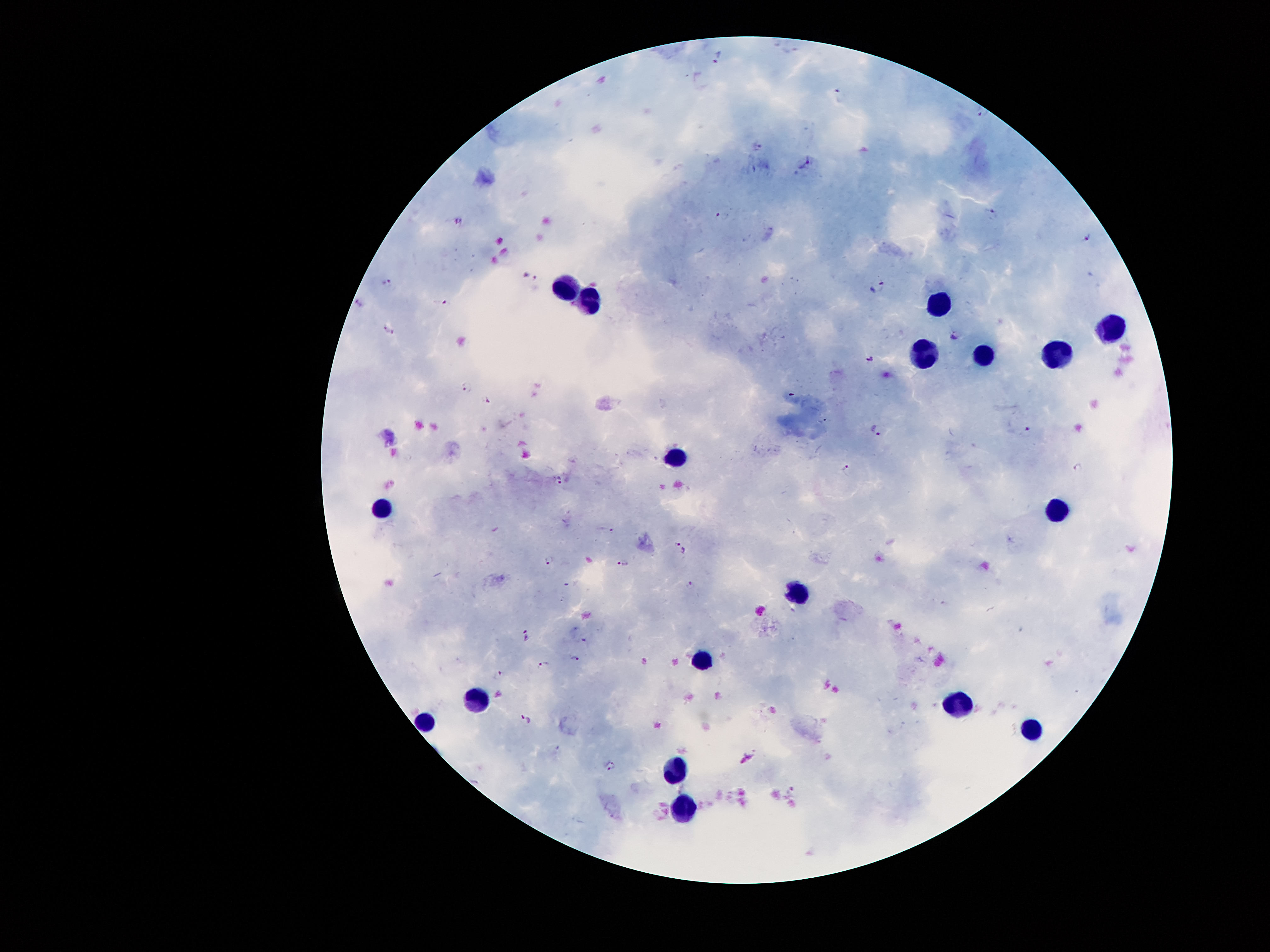 Approximate centers as {x, y} in pixels. Malaria parasite locations: {790, 50}, {719, 58}, {839, 94}, {984, 113}, {758, 146}, {805, 165}, {991, 212}, {721, 216}, {1086, 238}, {529, 279}, {389, 283}, {883, 287}, {358, 302}, {446, 303}, {390, 331}, {953, 336}, {869, 359}, {468, 387}, {486, 400}, {877, 429}, {1029, 431}, {1079, 468}, {846, 469}, {560, 480}, {612, 532}, {681, 546}, {549, 561}, {623, 563}, {690, 586}, {525, 634}, {584, 642}, {575, 659}, {543, 663}, {499, 675}, {527, 718}, {611, 766}. Leukocyte locations: {563, 290}, {938, 299}, {594, 302}, {1112, 325}, {983, 354}, {1056, 354}, {924, 361}, {676, 452}, {384, 509}, {1058, 514}, {797, 588}, {701, 660}, {482, 698}, {963, 702}, {425, 723}, {1033, 727}, {675, 766}, {681, 811}. Image is 1270×952 pixels. 100x magnification. Patient malaria status: infected with Plasmodium falciparum. One field from this slide. Thick blood smear. Smartphone photograph taken through the microscope eyepiece. Giemsa stain.